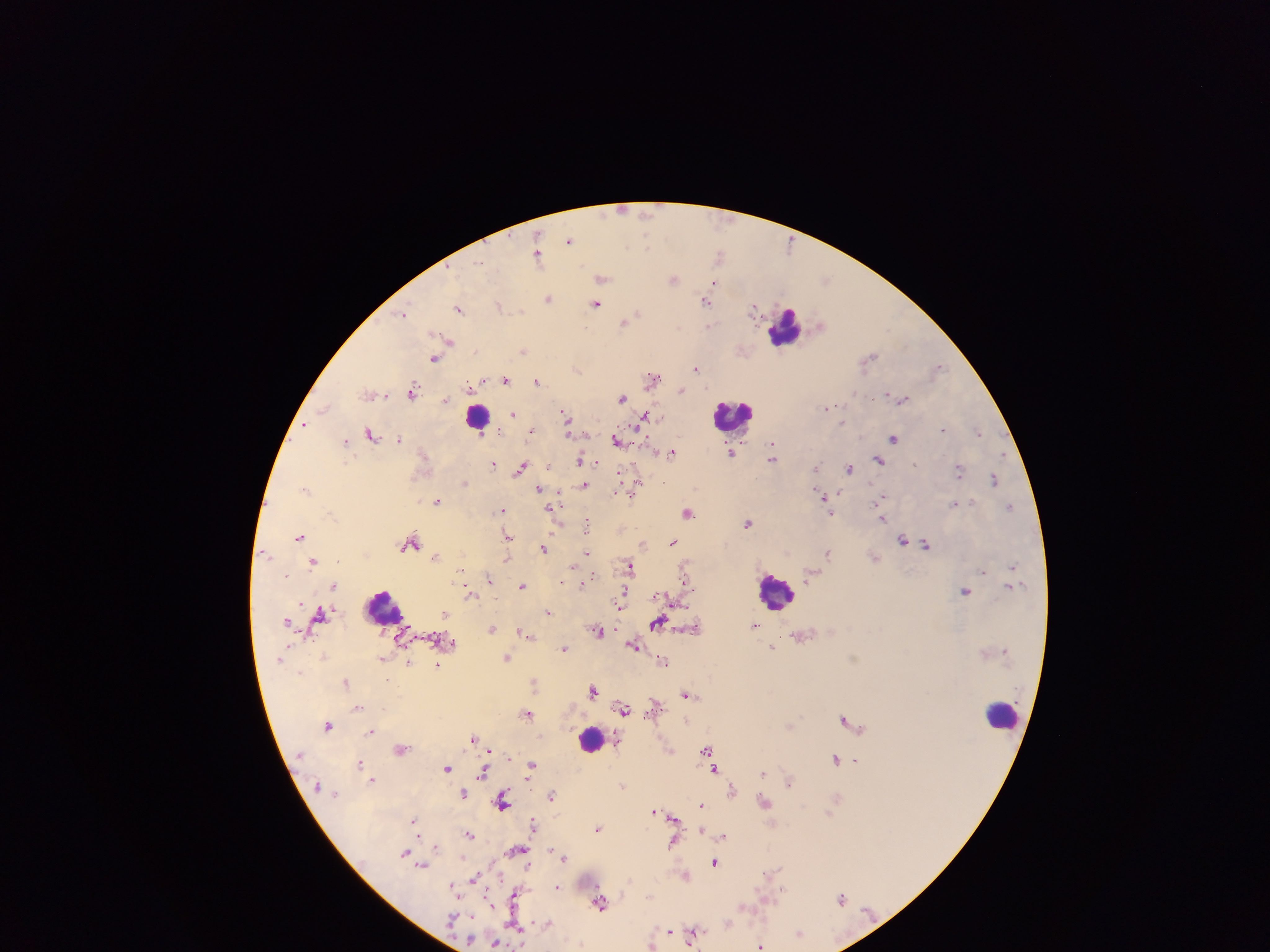

Approximate centers as {x, y} in pixels. Leukocyte locations: {786, 327}, {477, 415}, {733, 415}, {777, 592}, {384, 607}, {1004, 715}, {591, 739}. Plasmodium parasite locations: {623, 209}, {570, 239}, {792, 242}, {538, 253}, {720, 255}, {602, 278}, {674, 279}, {714, 282}, {549, 298}, {707, 300}, {597, 304}, {499, 305}, {755, 307}, {460, 309}, {403, 314}, {626, 321}, {710, 326}, {449, 342}, {523, 350}, {435, 357}, {868, 358}, {939, 366}, {577, 368}, {696, 368}, {653, 378}, {506, 380}, {482, 381}, {538, 381}, {473, 384}, {681, 389}, {413, 391}, {372, 393}, {887, 394}, {622, 396}, {903, 398}, {446, 401}, {829, 407}, {324, 408}, {513, 413}, {565, 413}, {645, 416}, {567, 421}, {305, 425}, {532, 430}, {943, 430}, {978, 431}, {371, 433}, {895, 437}, {400, 439}, {346, 440}, {618, 440}, {772, 443}, {672, 451}, {731, 452}, {773, 457}, {581, 460}, {880, 460}, {494, 463}, {916, 463}, {523, 467}, {816, 469}, {850, 469}, {959, 470}, {994, 477}, {465, 481}, {664, 481}, {585, 484}, {636, 484}, {307, 489}, {540, 489}, {619, 491}, {629, 493}, {824, 496}, {883, 496}, {438, 501}, {955, 503}, {1010, 505}, {553, 507}, {502, 510}, {831, 511}, {687, 512}, {883, 519}, {748, 522}, {588, 527}, {300, 535}, {507, 535}, {903, 539}, {410, 541}, {673, 542}, {643, 543}, {926, 544}, {545, 548}, {830, 551}, {587, 552}, {436, 556}, {874, 557}, {508, 558}, {314, 561}, {576, 565}, {686, 566}, {629, 567}, {1012, 567}, {461, 569}, {811, 574}, {489, 579}, {561, 581}, {686, 581}, {583, 583}, {334, 584}, {523, 585}, {1010, 585}, {966, 589}, {471, 594}, {620, 605}, {321, 613}, {548, 613}, {446, 614}, {288, 622}, {658, 623}, {755, 624}, {696, 627}, {493, 628}, {600, 630}, {524, 633}, {802, 635}, {634, 645}, {773, 647}, {565, 648}, {508, 656}, {382, 659}, {664, 660}, {409, 663}, {438, 663}, {535, 681}, {346, 682}, {593, 689}, {687, 692}, {654, 706}, {358, 708}, {623, 708}, {527, 713}, {845, 718}, {329, 725}, {789, 725}, {371, 731}, {475, 738}, {402, 748}, {489, 749}, {670, 749}, {708, 749}, {710, 756}, {508, 757}, {836, 758}, {855, 760}, {359, 762}, {532, 764}, {448, 767}, {714, 767}, {484, 772}, {764, 772}, {373, 779}, {788, 781}, {623, 786}, {733, 789}, {464, 793}, {551, 796}, {837, 799}, {764, 801}, {504, 802}, {703, 804}, {656, 811}, {673, 817}, {414, 819}, {534, 825}, {598, 828}, {702, 828}, {469, 834}, {724, 836}, {674, 840}, {723, 842}, {436, 846}, {516, 850}, {552, 850}, {406, 852}, {565, 857}, {715, 861}, {424, 865}, {528, 865}, {499, 875}, {686, 875}, {475, 878}, {453, 885}, {558, 886}, {784, 889}, {514, 895}, {842, 899}, {489, 900}, {600, 903}, {745, 906}, {473, 916}, {548, 923}, {728, 923}, {515, 927}, {670, 931}, {694, 933}, {800, 933}, {495, 942}, {652, 945}, {761, 945}. Collected in Ghana. Single field of view. Photographed through a microscope with a mobile-phone camera. Image is 1270×952 pixels. Thick blood smear.